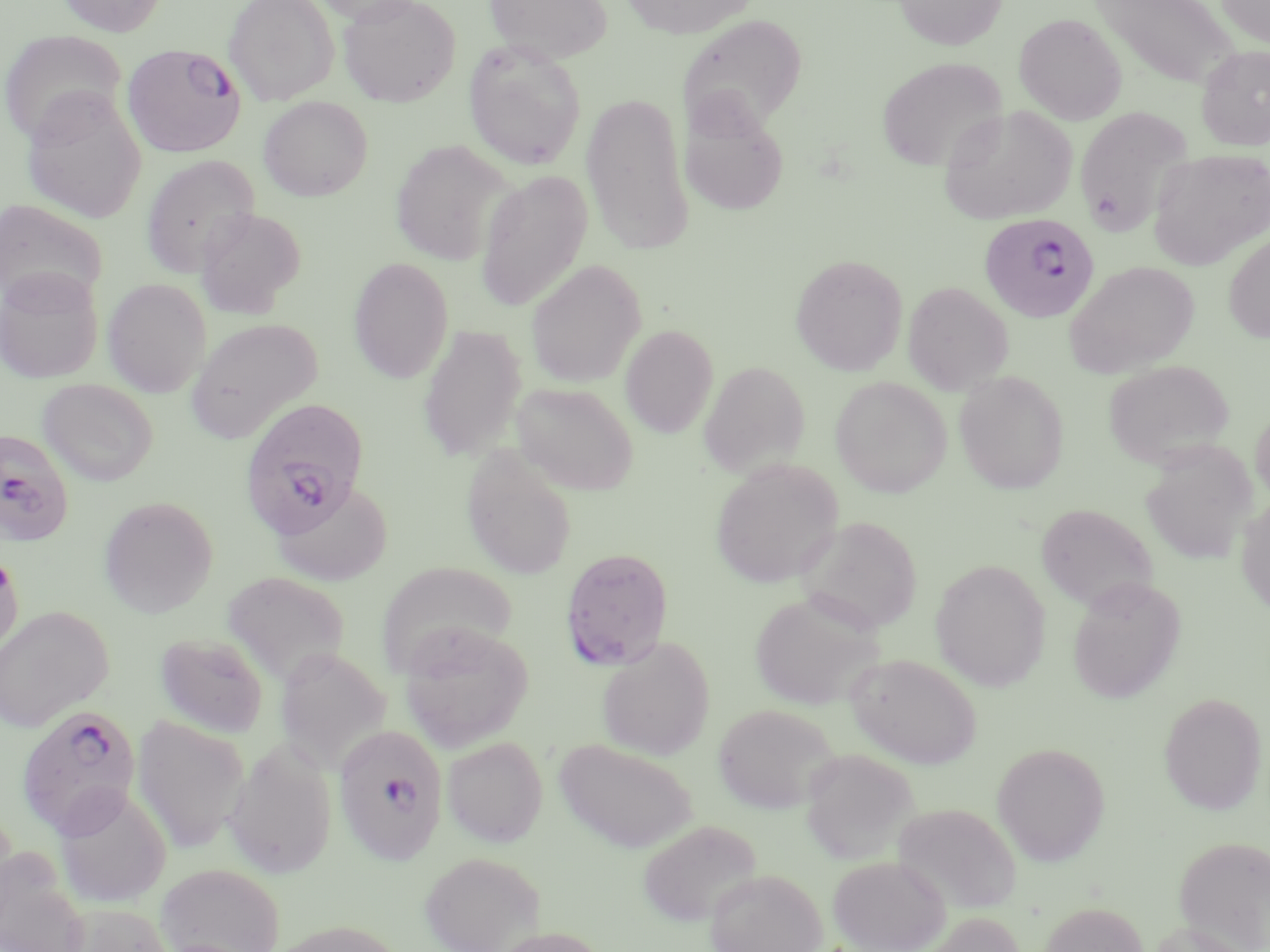
Approximate bounding boxes as (x1, y1, x2, y2) in pixels. Uninfected red blood cell locations: (56, 0, 167, 36), (224, 0, 338, 105), (312, 0, 428, 26), (338, 0, 461, 107), (483, 0, 613, 63), (620, 0, 758, 38), (894, 0, 1007, 51), (1213, 0, 1270, 49), (1090, 1, 1244, 90), (676, 13, 808, 137), (1014, 13, 1127, 125), (0, 30, 128, 144), (463, 39, 587, 170), (1195, 45, 1270, 150), (877, 56, 1007, 173), (21, 87, 146, 224), (580, 92, 694, 256), (258, 96, 373, 201), (680, 102, 789, 217), (938, 104, 1077, 226), (1074, 106, 1194, 236), (390, 140, 514, 265), (1148, 148, 1270, 270), (141, 154, 260, 278), (475, 169, 593, 312), (0, 199, 108, 310), (194, 207, 305, 318), (1223, 231, 1270, 344), (791, 253, 908, 376), (348, 257, 454, 383), (525, 259, 646, 388), (1065, 260, 1200, 378), (0, 267, 103, 384), (103, 278, 211, 397), (903, 281, 1013, 395), (187, 317, 323, 442), (418, 325, 527, 462), (620, 325, 719, 438), (1103, 359, 1236, 469), (699, 360, 810, 478), (954, 370, 1070, 494), (830, 377, 951, 498), (37, 378, 158, 486), (511, 382, 639, 496), (1249, 405, 1270, 508), (1141, 443, 1256, 566), (461, 446, 578, 580), (711, 459, 844, 589), (271, 478, 394, 587), (1236, 495, 1270, 617), (99, 496, 218, 618), (1036, 503, 1158, 614), (797, 516, 923, 634), (0, 549, 24, 657), (931, 559, 1050, 692), (376, 563, 516, 676), (220, 571, 351, 684), (1066, 576, 1186, 704), (749, 592, 883, 710), (0, 606, 114, 732), (398, 622, 535, 752), (155, 631, 269, 737), (597, 637, 715, 761), (275, 647, 391, 773), (845, 653, 982, 768), (1159, 692, 1268, 815), (713, 703, 839, 813), (133, 715, 249, 853), (442, 736, 548, 847), (554, 738, 698, 853), (223, 739, 338, 879), (992, 741, 1110, 866), (799, 748, 919, 864), (53, 784, 172, 908), (892, 802, 1021, 914), (636, 819, 763, 929), (1173, 835, 1270, 951), (0, 848, 89, 952), (419, 851, 545, 952), (828, 855, 950, 952), (156, 862, 285, 952), (705, 868, 827, 952), (1038, 900, 1149, 952), (60, 903, 174, 952), (914, 912, 1027, 952), (267, 919, 405, 952), (1146, 920, 1256, 952), (488, 926, 613, 952). Plasmodium falciparum-infected red blood cell locations: (123, 42, 246, 158), (978, 213, 1101, 323), (241, 400, 371, 541), (0, 428, 74, 546), (560, 547, 674, 670), (16, 704, 144, 840), (334, 723, 448, 865). Slide-level diagnosis: Plasmodium falciparum. 1000x magnification. May-Grünwald-Giemsa stain. One field of a larger specimen. Thin blood film. Image is 1270×952 pixels. Optical microscopy.